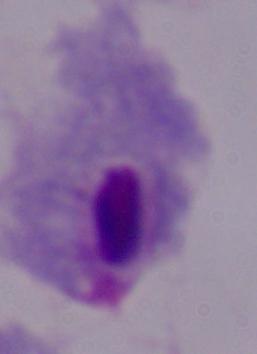
Summary:
  - Modality: photomicrograph
  - Identification: trichomonad
  - Magnification: 1000x